Give the position of every malaria parasite.
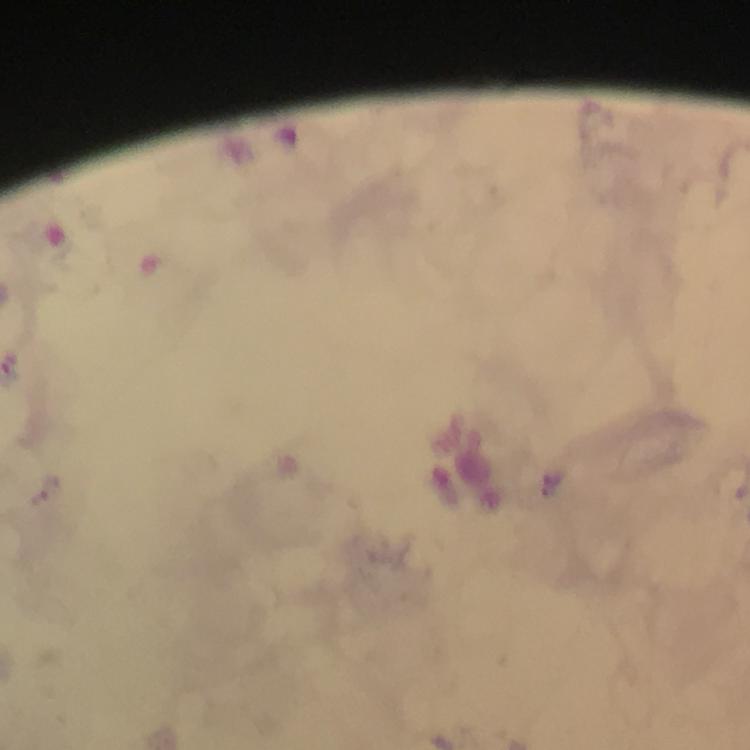

Approximate centers as {x, y} in pixels.
Malaria parasites: {51, 490}.

Summary:
  - Preparation: thick blood film
  - Stain: Giemsa
  - Capture: smartphone photograph through a microscope
  - Immersion oil: applied
  - Image size: 750×750 pixels
  - Magnification: 100x
  - Context: from a diagnostic examination for malaria
  - Cropped from: one field of view